Give the position of every leukocyte visible.
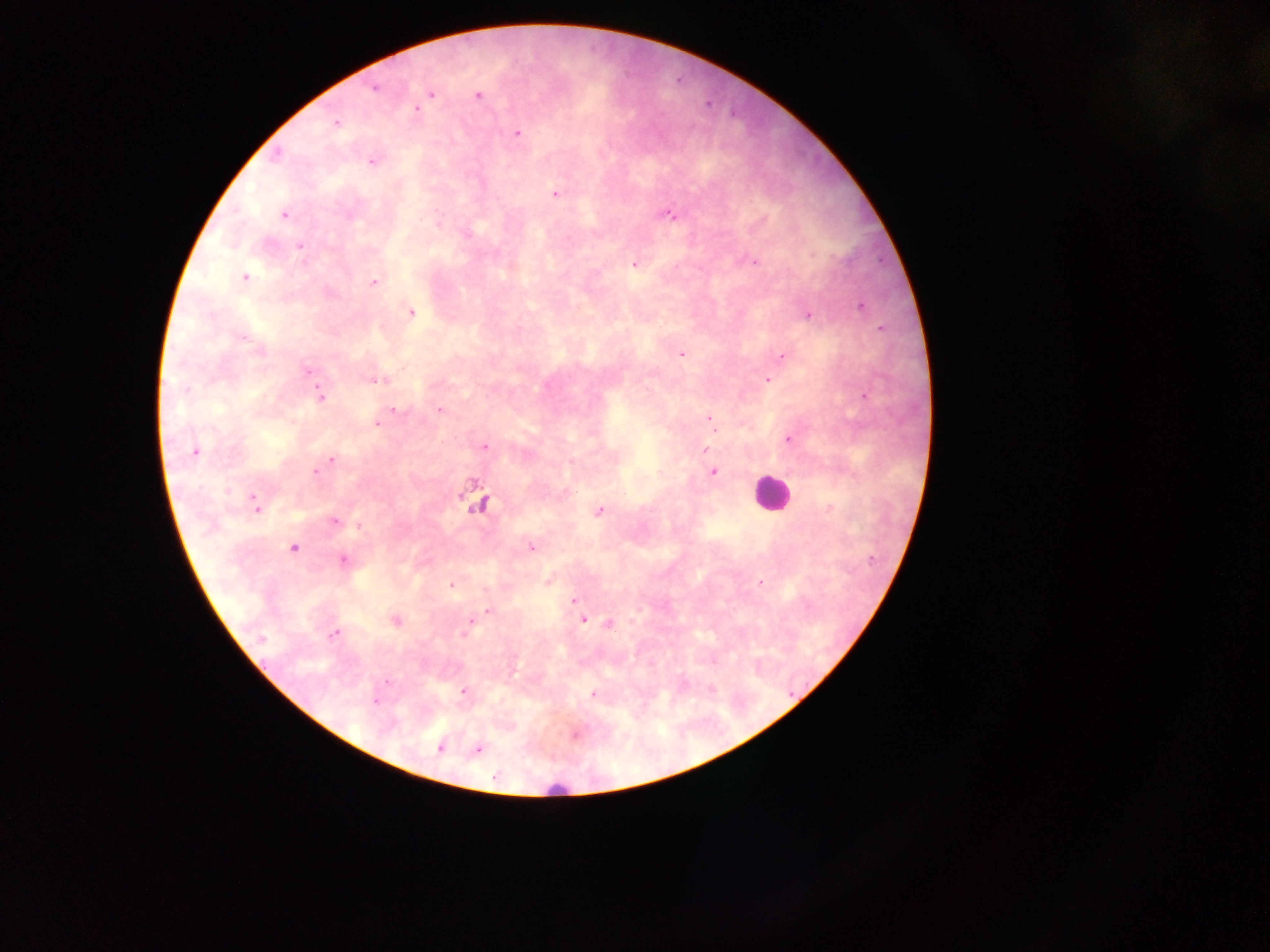
Approximate centers as {x, y} in pixels.
Leukocytes: {771, 494}, {557, 788}.

Malaria parasite locations: {375, 88}, {430, 93}, {477, 95}, {414, 108}, {335, 123}, {517, 132}, {275, 155}, {372, 161}, {554, 194}, {284, 214}, {669, 214}, {299, 247}, {752, 261}, {634, 264}, {244, 277}, {373, 281}, {861, 306}, {410, 312}, {806, 314}, {880, 328}, {681, 353}, {782, 355}, {309, 371}, {767, 379}, {375, 380}, {319, 395}, {864, 396}, {393, 409}, {440, 410}, {710, 417}, {376, 422}, {788, 439}, {484, 446}, {705, 449}, {194, 451}, {331, 460}, {316, 471}, {712, 471}, {479, 503}, {254, 504}, {598, 511}, {333, 520}, {359, 525}, {531, 547}, {292, 548}, {343, 559}, {548, 580}, {760, 582}, {450, 584}, {574, 600}, {489, 611}, {582, 619}, {395, 620}, {470, 622}, {608, 623}, {334, 633}, {462, 691}, {593, 693}, {375, 701}, {575, 734}, {440, 747}, {477, 749}. Thick blood smear. Mobile-phone photograph taken through the microscope. Image is 1270×952 pixels. Single field of view. Sample from Ghana.